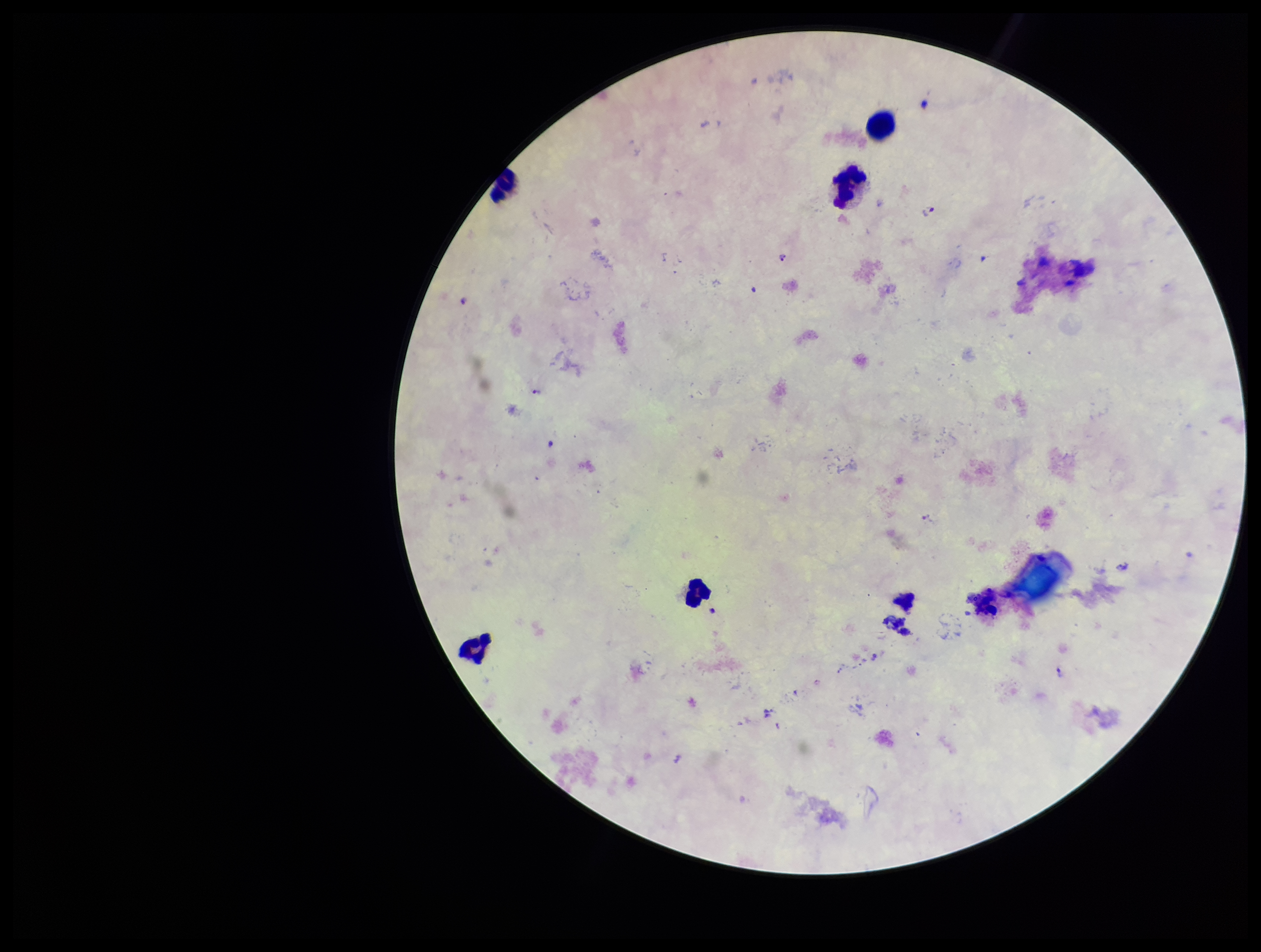
image size = 1261×952 pixels
stain = Giemsa
capture = smartphone photograph through the microscope eyepiece
field of view = single
patient malaria status = infected
Plasmodium parasites = seen
species reported for this patient = Plasmodium falciparum
parasite count = 4
leukocyte count = 6
preparation = thick